Describe the morphology of the erythrocytes.
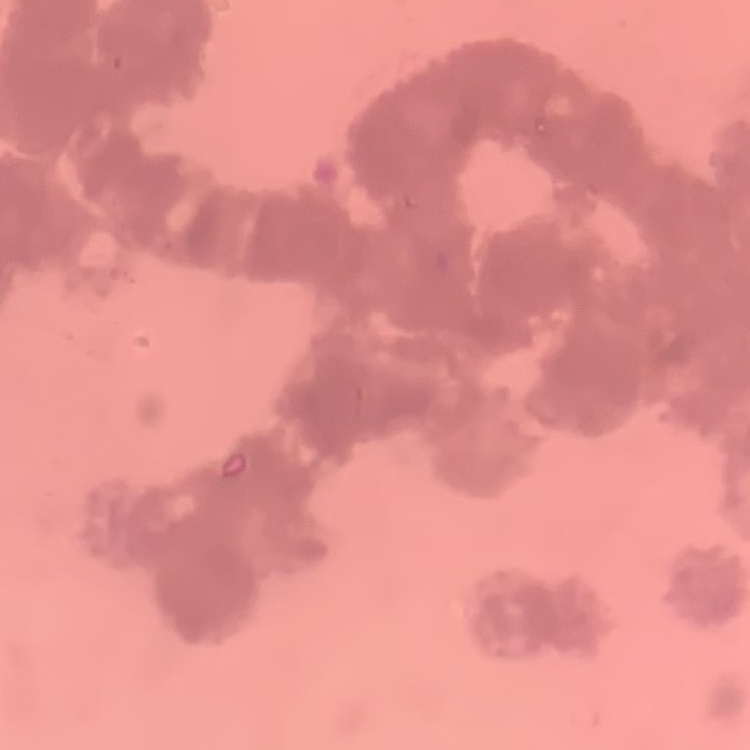
They show rouleaux formation.

image type = one tile cut from a larger photomicrograph
stain = Field's or Giemsa
preparation = thin blood smear